Classify this cell by malaria status.
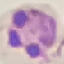

Parasitized.

Thin blood film. Giemsa stain. Photographed with a smartphone camera at the microscope eyepiece. Cell patch, automatically extracted from a larger field of view and resized to 64 × 64 pixels.